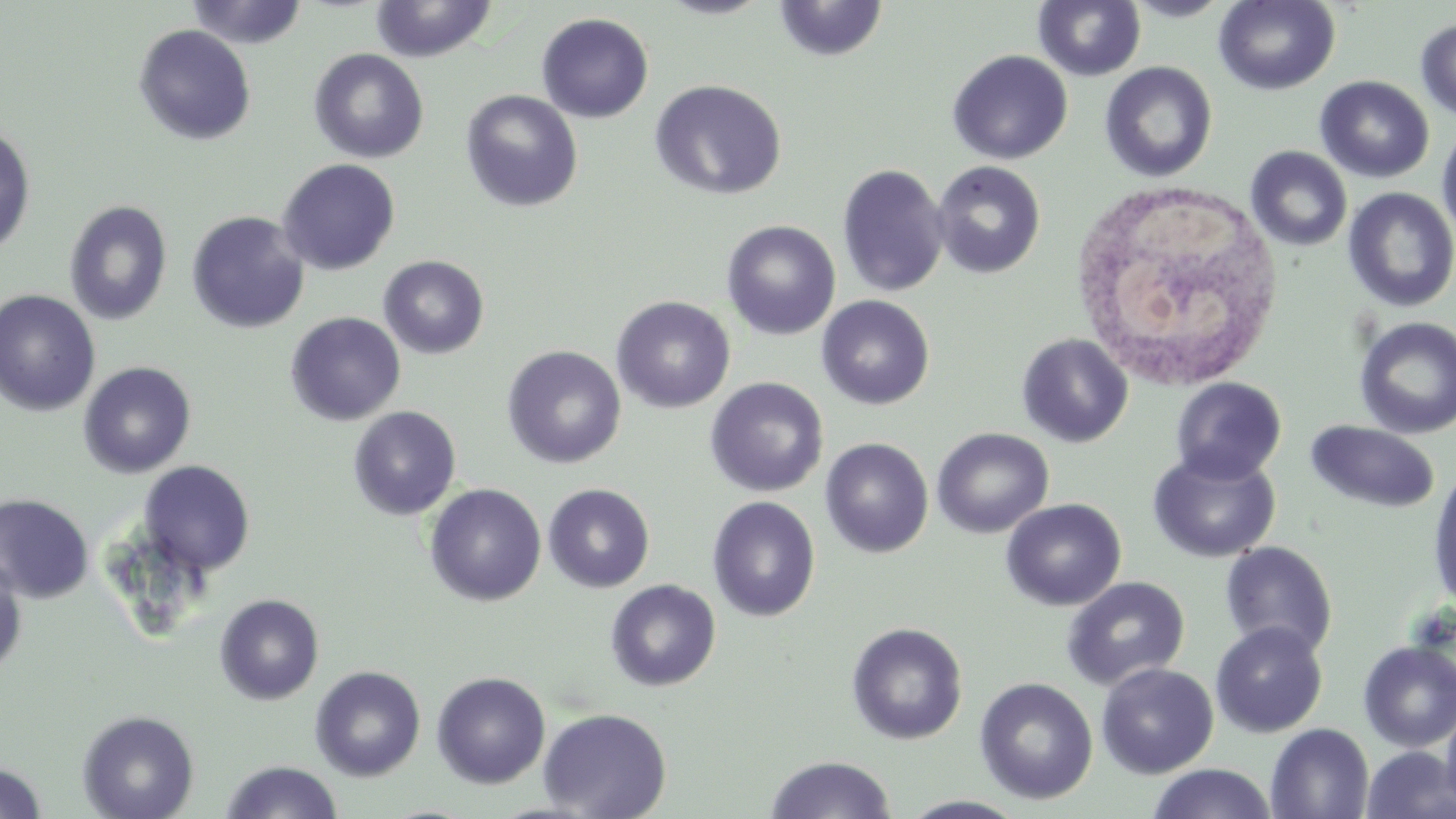

Summary:
  - Coordinate format: approximate bounding boxes as (x1, y1, x2, y2) in pixels
  - Uninfected red blood cell locations: (370, 0, 497, 62), (1034, 0, 1146, 81), (1124, 0, 1234, 22), (1215, 0, 1340, 95), (186, 1, 309, 49), (774, 1, 888, 63), (536, 12, 654, 123), (1415, 19, 1456, 123), (134, 24, 256, 146), (309, 48, 429, 164), (947, 49, 1073, 165), (1100, 62, 1217, 182), (1315, 75, 1434, 183), (649, 79, 787, 200), (461, 89, 583, 212), (0, 124, 36, 257), (1437, 124, 1456, 242), (1246, 146, 1352, 251), (277, 158, 401, 275), (932, 161, 1045, 279), (837, 163, 949, 298), (1343, 187, 1456, 311), (64, 200, 172, 325), (187, 211, 310, 334), (721, 220, 840, 341), (379, 255, 488, 359), (0, 289, 101, 416), (611, 295, 736, 414), (816, 295, 935, 410), (285, 311, 406, 426), (1354, 317, 1456, 439), (1017, 333, 1133, 447), (502, 345, 627, 469), (78, 361, 197, 479), (705, 377, 829, 497), (1171, 377, 1286, 485), (348, 406, 461, 520), (1306, 420, 1440, 513), (932, 427, 1054, 538), (820, 437, 934, 558), (1148, 450, 1281, 564), (139, 460, 255, 576), (1427, 463, 1456, 614), (425, 483, 546, 606), (543, 483, 655, 593), (0, 494, 94, 603), (707, 496, 821, 621), (1001, 498, 1126, 611), (1220, 541, 1338, 658), (0, 558, 27, 677), (1062, 576, 1190, 691), (605, 579, 721, 691), (214, 593, 324, 705), (846, 622, 967, 745), (1210, 622, 1328, 738), (1357, 641, 1456, 752), (1097, 662, 1219, 779), (310, 665, 426, 781), (431, 671, 551, 789), (975, 677, 1098, 804), (1441, 706, 1456, 816), (537, 707, 672, 818), (77, 709, 200, 819), (1266, 724, 1374, 819), (1361, 746, 1456, 819), (766, 755, 896, 818), (220, 761, 344, 819), (0, 762, 47, 819), (1146, 764, 1277, 819)
  - White blood cell locations: (1068, 177, 1286, 392)
  - Slide-level diagnosis: no evidence of blood parasites
  - Modality: light microscopy
  - Magnification: 1000x
  - Field of view: one of a larger specimen
  - Preparation: thin blood smear
  - Image size: 1456×819 pixels
  - Stain: May-Grünwald-Giemsa